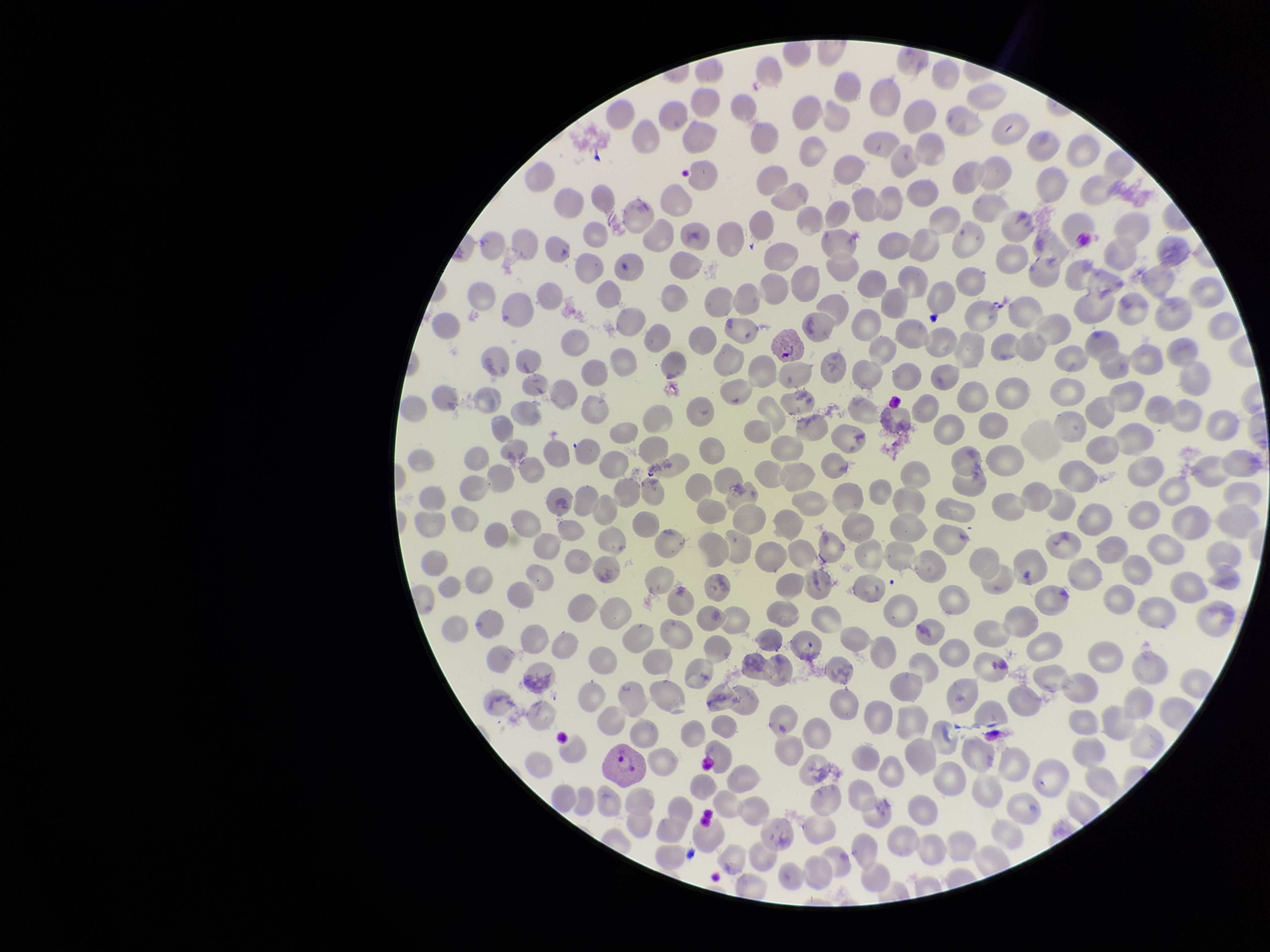
Summary:
  - Parasitized red blood cell count: 1
  - Stain: Giemsa
  - Preparation: thin
  - Capture: smartphone photograph through the microscope eyepiece
  - Parasitized red blood cells: seen
  - Image size: 1270×952 pixels
  - Patient malaria status: infected
  - Field of view: one from this slide
  - Species reported for this patient: Plasmodium vivax
  - Red blood cell count: 301